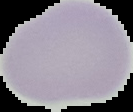
image size = 133×112 pixels
preparation = thin blood film
malaria status = uninfected
image type = segmented cell region with the area outside set to black